Identify the preparation type.
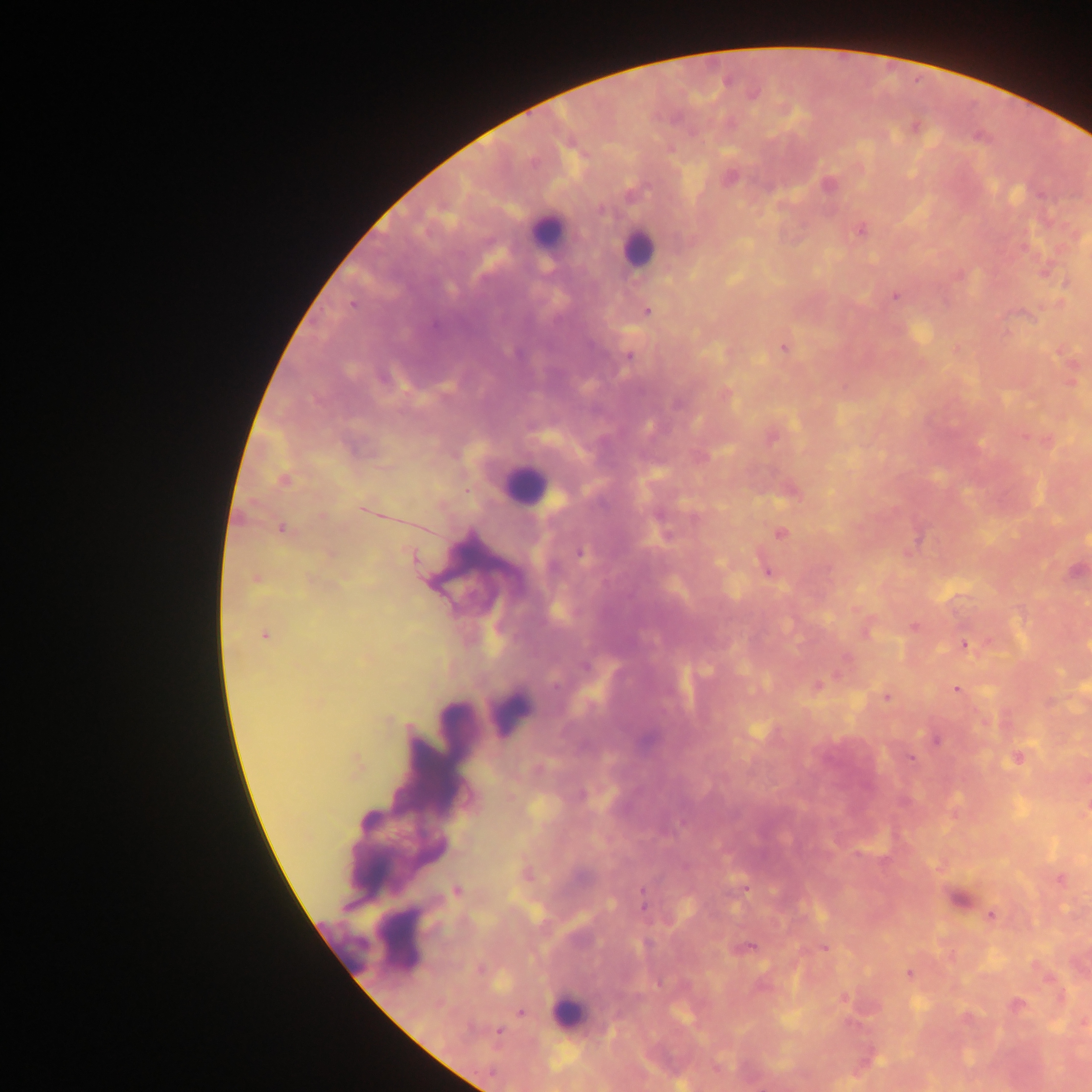
Thick blood film.

leukocyte locations = approximate centers as (x, y) in pixels: (544, 233), (638, 247), (525, 485), (510, 712), (457, 722), (400, 939), (340, 940), (570, 1012)
Plasmodium parasite locations = approximate centers as (x, y) in pixels: (917, 82), (916, 128), (729, 177), (828, 185), (1039, 195), (602, 210), (858, 230), (894, 296), (646, 310), (783, 348), (629, 354), (724, 393), (1026, 435), (284, 479), (467, 491), (365, 511), (322, 517), (283, 528), (780, 534), (582, 553), (765, 568), (264, 634), (963, 645), (816, 685), (957, 689), (911, 757), (1016, 757), (745, 889), (455, 890), (643, 890), (644, 907), (990, 914), (752, 946), (823, 948), (908, 973), (521, 1012), (499, 1031)
image size = 1092×1092 pixels
capture = mobile-phone photograph through a microscope
country = Ghana
field of view = single